Locate and identify every blood parasite.
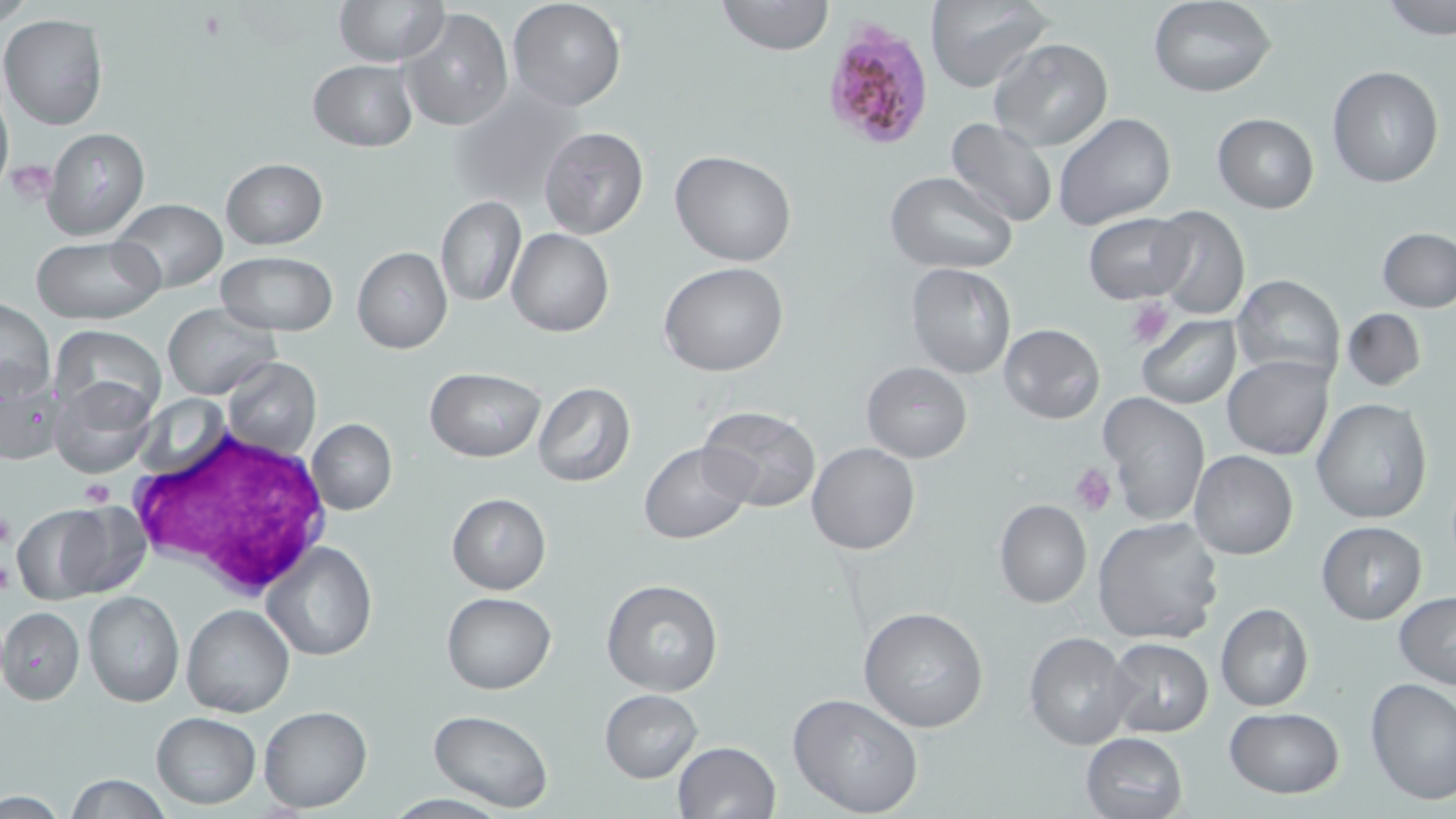

Approximate bounding boxes as (x1, y1, x2, y2) in pixels.
Plasmodium falciparum-infected red blood cells: (818, 18, 940, 154).
No Plasmodium ovale, Plasmodium malariae, Plasmodium vivax, Babesia divergens, or Trypanosoma brucei observed.

slide-level diagnosis = Plasmodium falciparum
field of view = single
white blood cell locations = approximate bounding boxes as (x1, y1, x2, y2) in pixels: (125, 426, 333, 598)
modality = light microscopy
uninfected red blood cell locations = approximate bounding boxes as (x1, y1, x2, y2) in pixels: (507, 0, 628, 112), (716, 0, 833, 56), (924, 0, 1052, 93), (1380, 0, 1456, 39), (335, 1, 448, 67), (1148, 2, 1278, 99), (400, 7, 514, 132), (1, 15, 111, 130), (990, 37, 1114, 151), (308, 60, 417, 151), (1327, 64, 1443, 188), (448, 86, 584, 201), (0, 87, 13, 193), (1052, 112, 1177, 229), (1212, 112, 1320, 214), (944, 118, 1059, 229), (539, 126, 648, 239), (41, 127, 151, 241), (669, 150, 796, 266), (220, 158, 327, 250), (885, 171, 1018, 272), (436, 196, 524, 307), (111, 199, 226, 294), (1147, 206, 1251, 320), (1083, 213, 1194, 305), (1377, 227, 1456, 313), (506, 228, 614, 337), (33, 235, 162, 323), (351, 246, 453, 354), (214, 251, 337, 336), (659, 262, 789, 377), (905, 263, 1018, 380), (1230, 273, 1345, 381), (1, 299, 55, 402), (162, 302, 282, 401), (1342, 308, 1426, 392), (1135, 315, 1241, 409), (51, 324, 165, 419), (999, 324, 1106, 424), (1222, 355, 1335, 461), (223, 359, 321, 459), (0, 360, 63, 465), (860, 362, 972, 463), (423, 367, 546, 461), (49, 378, 156, 477), (533, 383, 635, 487), (1099, 393, 1210, 527), (1312, 398, 1435, 523), (696, 407, 822, 514), (307, 419, 397, 515), (638, 442, 752, 544), (807, 442, 921, 555), (1190, 452, 1297, 560), (446, 492, 550, 595), (994, 499, 1091, 608), (52, 500, 151, 598), (10, 504, 115, 603), (1093, 517, 1225, 645), (1316, 521, 1426, 625), (263, 541, 378, 661), (601, 578, 724, 696), (82, 591, 185, 708), (1394, 591, 1456, 692), (441, 592, 556, 694), (1215, 603, 1314, 712), (182, 604, 295, 718), (858, 605, 988, 734), (1, 607, 84, 705), (1024, 632, 1137, 750), (1105, 637, 1215, 739), (1364, 679, 1456, 807), (600, 688, 703, 782), (787, 692, 925, 818), (259, 705, 372, 812), (1223, 707, 1346, 797), (428, 709, 552, 813), (151, 712, 260, 808), (1079, 733, 1188, 819), (671, 740, 781, 819), (67, 775, 172, 817)
stain = May-Grünwald-Giemsa
platelet locations = approximate bounding boxes as (x1, y1, x2, y2) in pixels: (7, 158, 53, 204), (1127, 298, 1175, 350), (1071, 464, 1115, 515), (79, 479, 113, 508), (0, 504, 17, 552), (0, 554, 15, 597)
image size = 1456×819 pixels
magnification = 1000x
preparation = thin blood smear